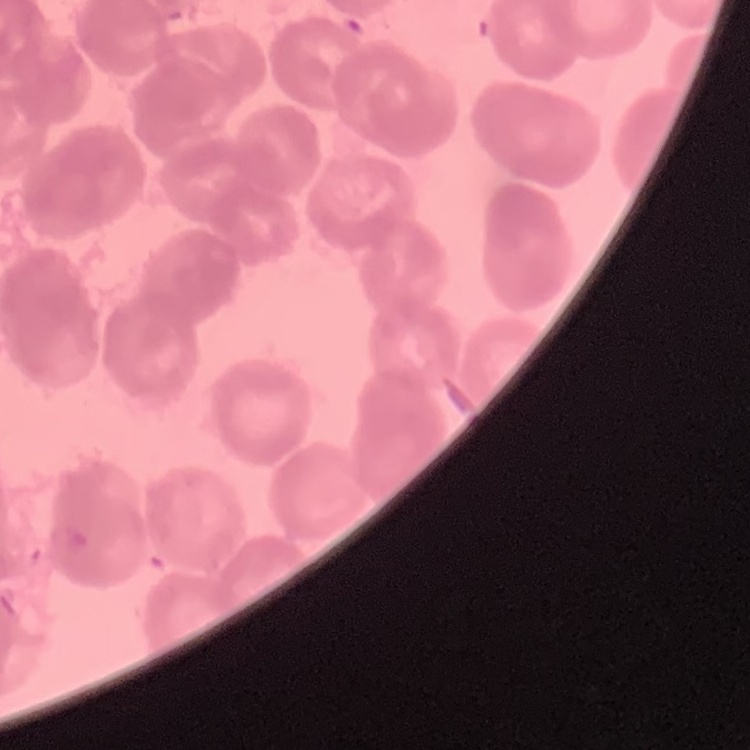
Summary:
  - Erythrocyte morphology: rouleaux formation
  - Preparation: thin blood smear
  - Stain: Field's or Giemsa
  - Image type: one tile cut from a larger photomicrograph